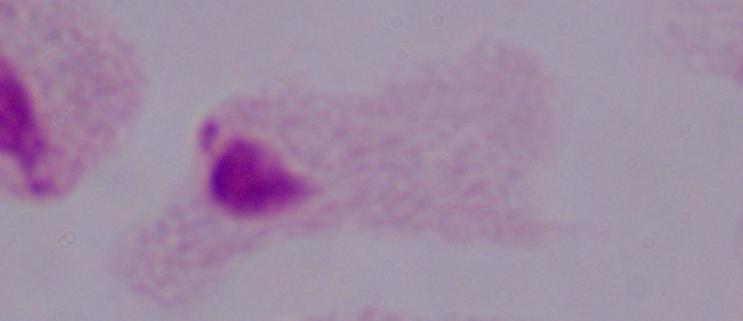
Summary:
  - Modality: micrograph
  - Identification: trichomonad
  - Magnification: 1000x